Identify the parasite.
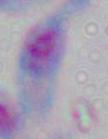
This is Toxoplasma gondii.

Summary:
  - Magnification: 1000x
  - Modality: micrograph